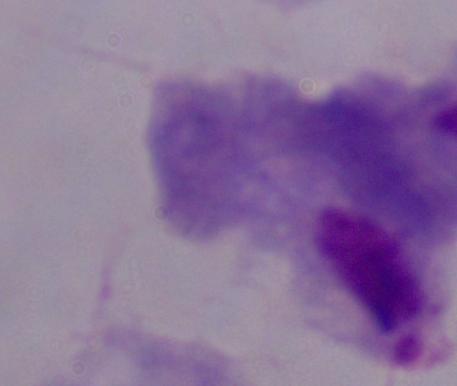
modality = micrograph
identification = trichomonad
magnification = 1000x